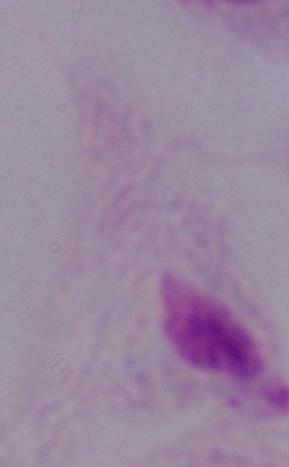

Summary:
  - Identification: trichomonad
  - Magnification: 1000x
  - Modality: photomicrograph